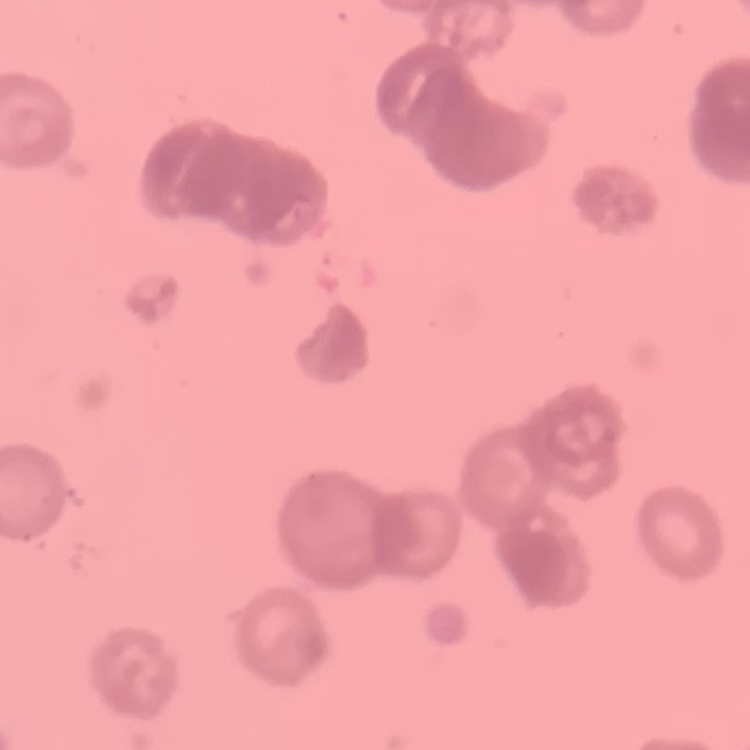
The erythrocytes show rouleaux formation. Thin peripheral smear. Stained with either Field's or Giemsa. One tile cut from a larger photomicrograph.